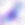

Summary:
  - Magnification: 400x
  - Modality: photomicrograph
  - Identification: Toxoplasma gondii